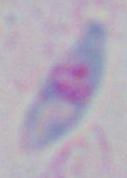

Toxoplasma gondii is shown. Captured at 1000x magnification. Photomicrograph.